Identify the preparation type.
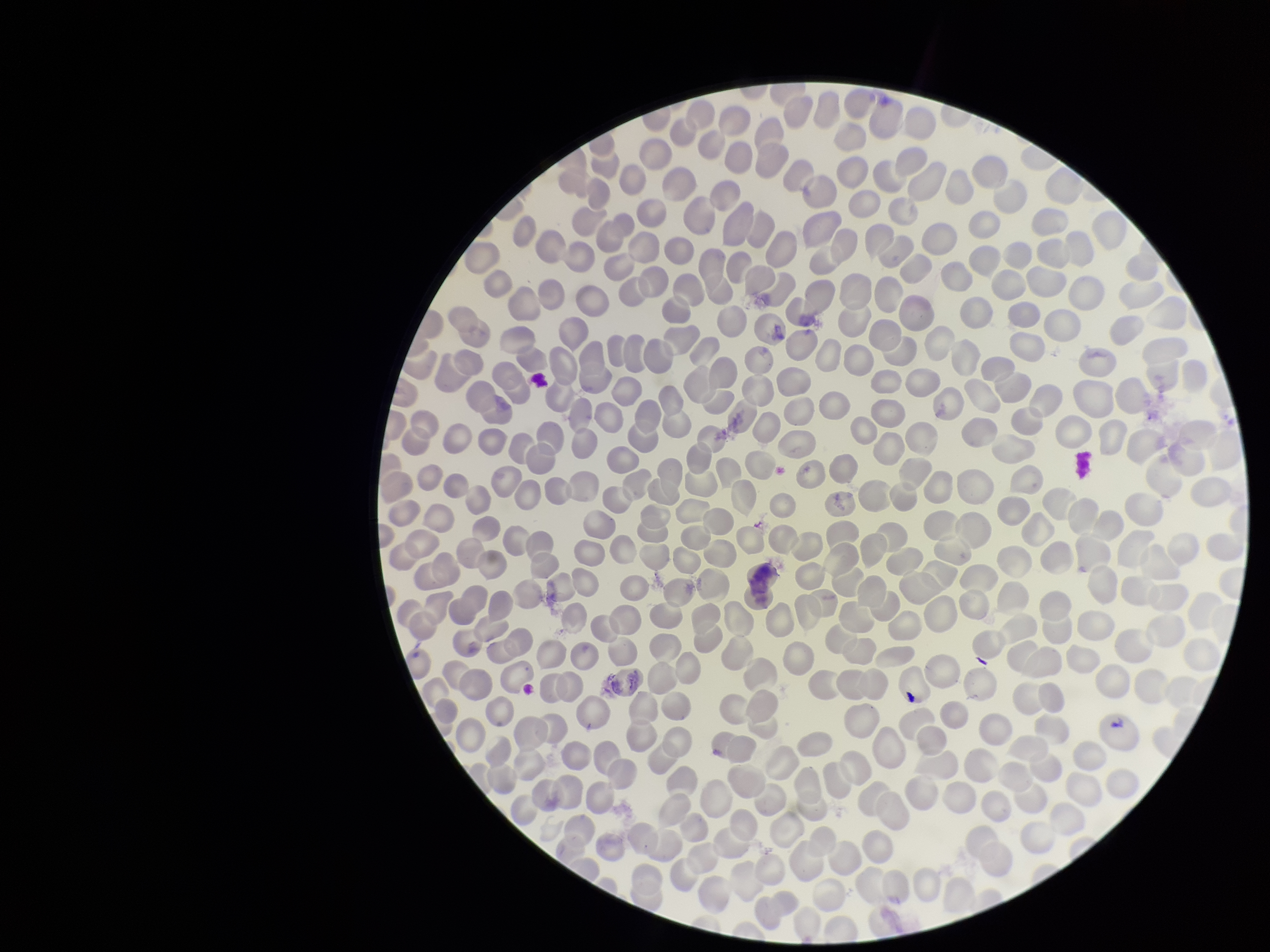

A thin smear.

{
  "stain": "Giemsa",
  "capture": "smartphone photograph through the microscope eyepiece",
  "parasitized_red_blood_cell_count": 0,
  "image_size": "1270×952 pixels",
  "field_of_view": "one from this slide",
  "patient_malaria_status": "negative",
  "red_blood_cell_count": 293,
  "parasitized_red_blood_cells": "none detected"
}